Report the malaria status of this cell.
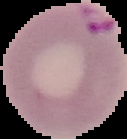

Parasitized.

preparation = thin blood film
image type = segmented cell region on a black background
image size = 127×139 pixels